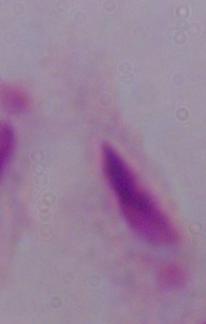
Summary:
  - Magnification: 1000x
  - Identification: trichomonad
  - Modality: photomicrograph